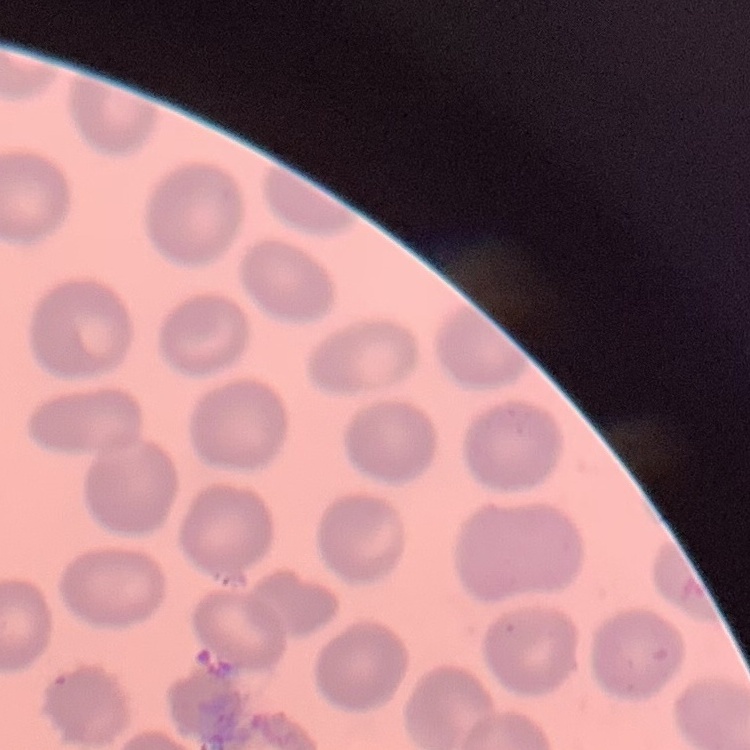

red blood cell morphology = no rouleaux formation
image type = one tile cut from a larger photomicrograph
stain = Field's or Giemsa
preparation = thin peripheral smear